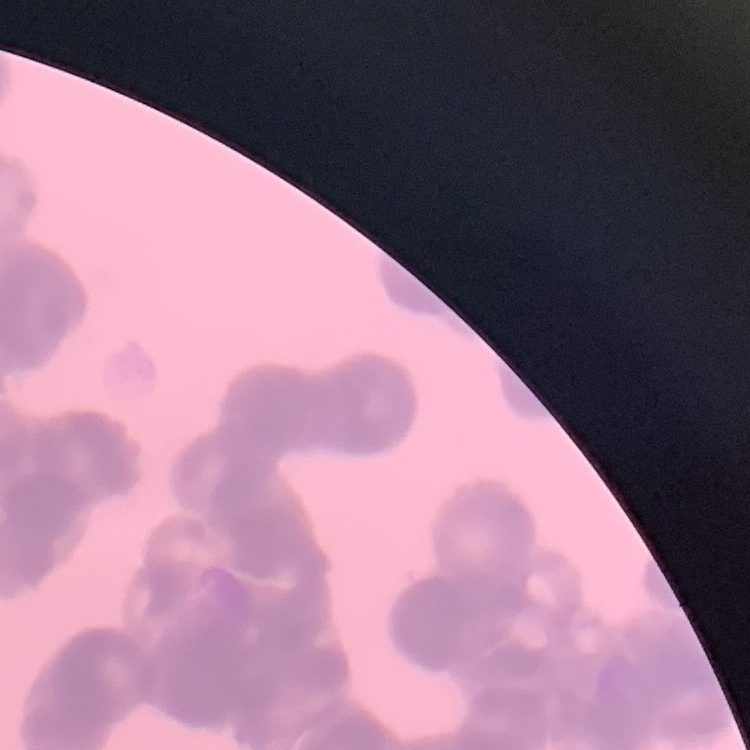
red blood cell morphology = rouleaux formation
preparation = thin blood film
stain = Field's or Giemsa
image type = square crop of a larger photomicrograph